Describe the morphology of the erythrocytes.
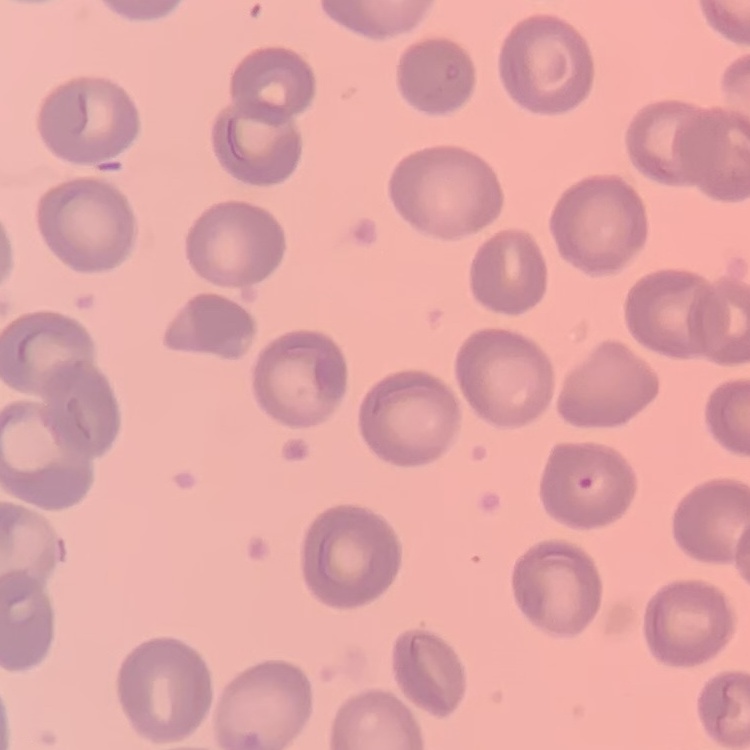
They show no rouleaux formation.

image type = square crop of a larger photomicrograph
preparation = thin blood smear
stain = Field's or Giemsa